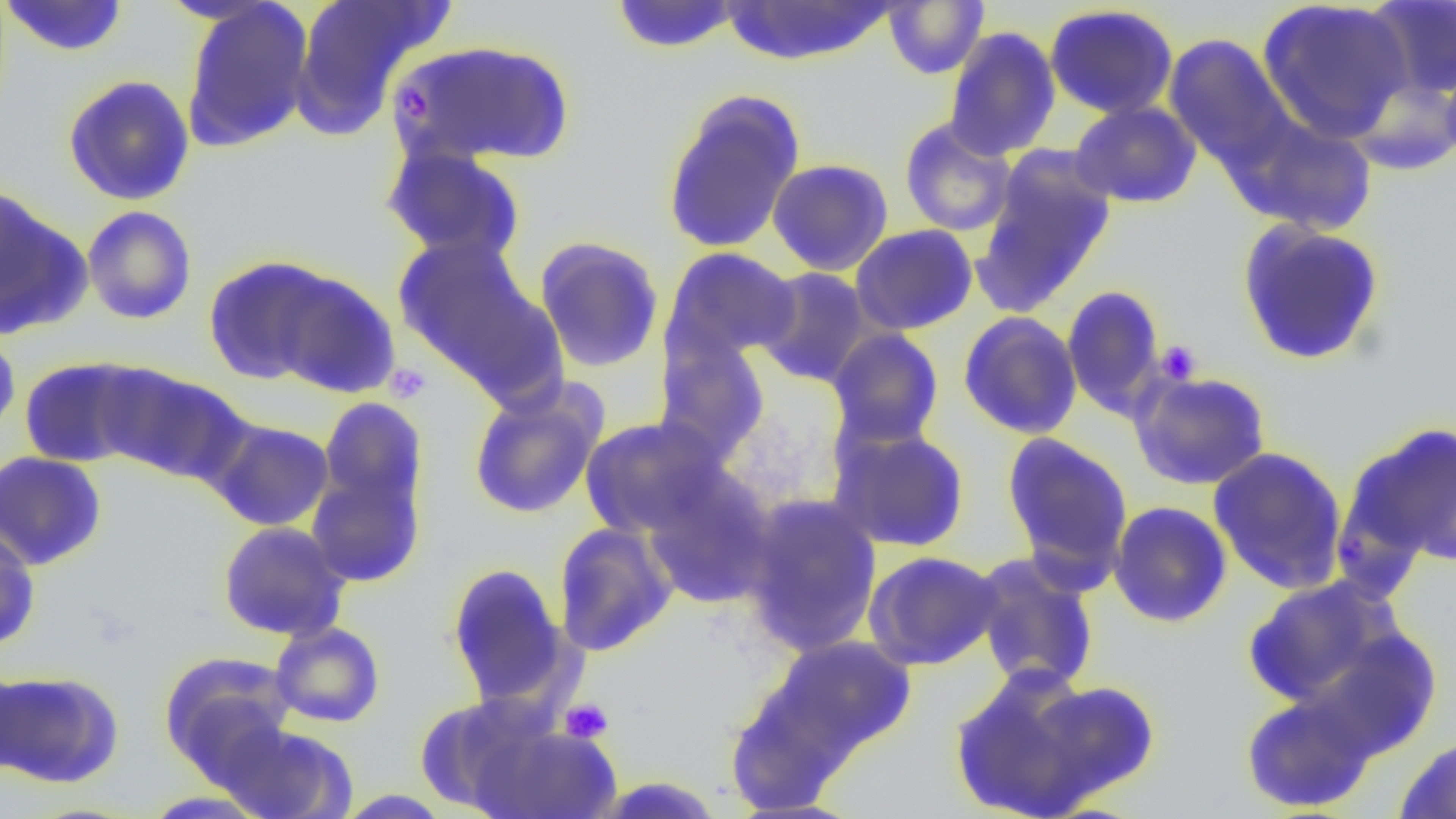
slide-level diagnosis = negative for blood parasites
image size = 1456×819 pixels
field of view = single
magnification = 1000x
preparation = thin blood film
modality = optical microscopy
platelet locations = approximate bounding boxes as (x1, y1, x2, y2) in pixels: (392, 83, 437, 124), (1156, 340, 1203, 384), (385, 363, 431, 403), (560, 698, 613, 742)
uninfected red blood cell locations = approximate bounding boxes as (x1, y1, x2, y2) in pixels: (289, 0, 452, 138), (719, 0, 898, 68), (1257, 0, 1414, 142), (1365, 0, 1456, 101), (1, 1, 130, 58), (179, 1, 315, 154), (609, 1, 744, 53), (883, 1, 989, 79), (1043, 4, 1180, 120), (943, 26, 1061, 161), (1163, 33, 1294, 171), (390, 39, 575, 167), (1440, 54, 1456, 169), (62, 75, 195, 206), (1347, 76, 1455, 177), (660, 90, 806, 256), (1069, 101, 1202, 209), (1234, 114, 1378, 236), (899, 117, 1017, 237), (382, 143, 526, 264), (973, 148, 1117, 315), (767, 158, 894, 276), (0, 187, 90, 339), (81, 205, 197, 325), (1236, 219, 1386, 366), (850, 224, 978, 335), (392, 235, 549, 388), (534, 235, 665, 374), (662, 247, 800, 365), (203, 255, 339, 385), (756, 267, 874, 387), (268, 268, 401, 400), (1061, 284, 1167, 420), (958, 310, 1083, 440), (826, 327, 945, 447), (0, 330, 21, 441), (654, 336, 770, 463), (18, 356, 153, 469), (100, 365, 250, 486), (1130, 371, 1272, 490), (468, 384, 606, 520), (318, 398, 427, 515), (579, 415, 727, 539), (206, 418, 336, 531), (1339, 423, 1456, 575), (829, 425, 970, 553), (1001, 432, 1134, 583), (1207, 446, 1349, 594), (0, 450, 108, 571), (307, 465, 426, 588), (642, 473, 776, 610), (740, 494, 883, 657), (1108, 501, 1233, 628), (217, 520, 350, 642), (552, 521, 678, 657), (0, 525, 41, 651), (863, 550, 1003, 671), (969, 552, 1101, 694), (445, 561, 570, 709), (1243, 576, 1402, 708), (270, 621, 385, 727), (762, 636, 918, 763), (160, 650, 298, 780), (0, 663, 29, 779), (946, 664, 1117, 818), (0, 669, 123, 787), (1019, 676, 1162, 808), (1240, 688, 1377, 814), (415, 694, 556, 814), (471, 720, 623, 818), (217, 721, 359, 819), (1394, 735, 1456, 818), (138, 790, 272, 818), (333, 790, 453, 818)